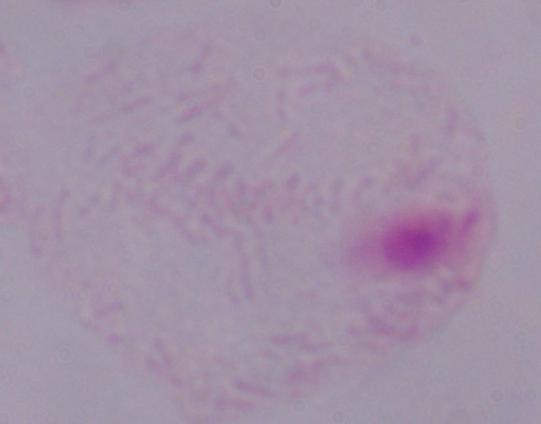

identification = trichomonad
modality = micrograph
magnification = 1000x